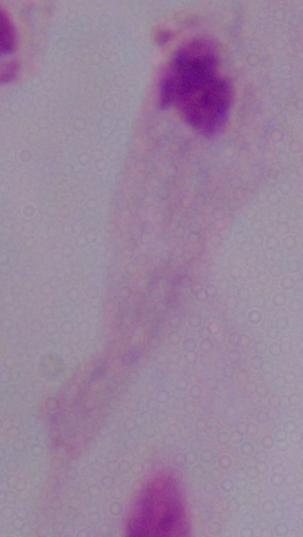

Summary:
  - Modality: micrograph
  - Identification: trichomonad
  - Magnification: 1000x